State which parasite is depicted.
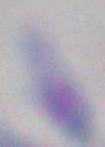
This is Toxoplasma gondii.

Photomicrograph. 1000x magnification.